Assess this cell for malaria.
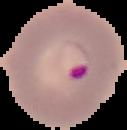
It is parasitized.

image type = segmented cell region on a black background
preparation = thin blood smear
image size = 127×130 pixels